Report the malaria status of this cell.
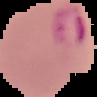

Parasitized.

image type = segmented cell region with the area outside set to black
image size = 97×97 pixels
preparation = thin blood smear